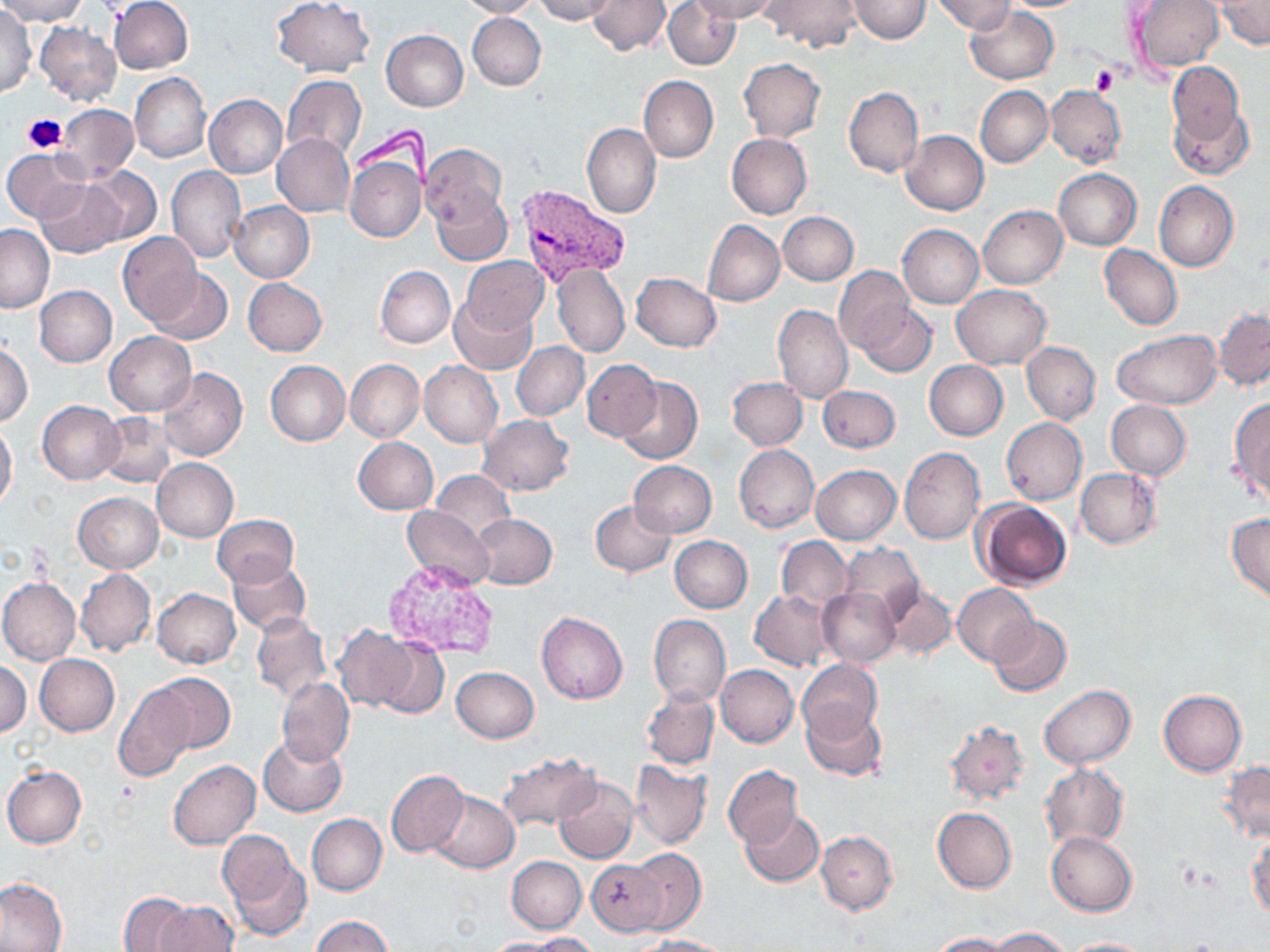

Summary:
  - Coordinate format: approximate bounding boxes as [x1, y1, x2, y2] in pixels
  - Platelet locations: [1090, 66, 1122, 94], [23, 113, 68, 153]
  - Uninfected red blood cell locations: [0, 0, 87, 24], [108, 0, 193, 74], [272, 0, 374, 76], [457, 0, 541, 18], [533, 0, 618, 23], [589, 0, 672, 55], [663, 0, 741, 70], [691, 0, 779, 22], [760, 0, 862, 53], [848, 0, 932, 42], [930, 0, 1014, 34], [1130, 1, 1222, 72], [1215, 1, 1269, 50], [967, 5, 1059, 83], [0, 8, 37, 98], [467, 13, 546, 90], [35, 21, 122, 105], [381, 30, 468, 112], [739, 58, 825, 141], [1168, 61, 1244, 145], [130, 72, 210, 162], [282, 75, 366, 160], [638, 76, 717, 162], [844, 85, 924, 178], [975, 85, 1053, 167], [1046, 85, 1126, 167], [204, 94, 288, 179], [58, 104, 137, 181], [1170, 104, 1254, 178], [583, 123, 661, 218], [900, 130, 989, 215], [272, 133, 355, 217], [726, 133, 811, 219], [420, 144, 507, 228], [3, 148, 90, 222], [345, 156, 426, 242], [86, 165, 162, 246], [167, 166, 246, 263], [1055, 169, 1142, 250], [36, 179, 127, 259], [1154, 180, 1238, 272], [431, 190, 513, 265], [230, 202, 314, 283], [977, 205, 1068, 289], [777, 211, 859, 285], [702, 220, 784, 306], [0, 224, 54, 312], [898, 224, 984, 308], [118, 232, 202, 326], [1100, 245, 1182, 330], [460, 257, 549, 334], [369, 264, 447, 428], [552, 264, 631, 358], [376, 266, 455, 347], [834, 266, 915, 355], [147, 268, 233, 346], [631, 273, 721, 351], [243, 277, 327, 356], [34, 285, 117, 367], [951, 285, 1052, 368], [449, 297, 539, 373], [856, 303, 937, 378], [773, 304, 853, 403], [1214, 308, 1270, 388], [1113, 330, 1222, 410], [104, 332, 196, 416], [511, 341, 589, 421], [1022, 342, 1100, 424], [0, 344, 32, 426], [265, 360, 350, 446], [346, 360, 424, 441], [582, 360, 661, 441], [420, 361, 503, 447], [924, 361, 1007, 440], [159, 367, 247, 461], [616, 375, 703, 465], [726, 376, 807, 450], [818, 385, 902, 453], [1229, 398, 1270, 500], [38, 400, 124, 485], [1106, 401, 1191, 479], [97, 413, 176, 487], [476, 414, 575, 496], [1002, 418, 1087, 505], [0, 422, 18, 508], [354, 436, 439, 514], [734, 444, 819, 533], [899, 447, 984, 545], [152, 457, 238, 542], [628, 460, 717, 537], [811, 465, 901, 544], [1076, 469, 1160, 548], [432, 471, 515, 544], [73, 493, 163, 573], [974, 499, 1073, 590], [591, 500, 676, 576], [404, 505, 494, 593], [1228, 513, 1270, 602], [471, 514, 557, 588], [213, 515, 297, 587], [775, 535, 852, 611], [669, 536, 752, 613], [837, 545, 925, 621], [229, 559, 310, 635], [75, 568, 156, 656], [0, 578, 80, 665], [883, 580, 956, 659], [954, 583, 1038, 666], [817, 587, 901, 667], [152, 588, 241, 668], [750, 591, 834, 671], [251, 612, 331, 702], [537, 612, 627, 704], [649, 615, 730, 707], [988, 617, 1071, 697], [331, 626, 418, 711], [372, 637, 448, 719], [35, 654, 119, 735], [798, 659, 881, 743], [0, 661, 30, 737], [716, 664, 799, 747], [451, 666, 539, 742], [151, 672, 234, 754], [276, 677, 354, 766], [115, 682, 194, 781], [1039, 685, 1136, 767], [642, 688, 719, 769], [1159, 690, 1247, 776], [801, 702, 885, 782], [943, 720, 1031, 806], [258, 735, 347, 817], [498, 752, 600, 830], [1221, 759, 1270, 843], [169, 761, 260, 849], [631, 761, 711, 849], [1039, 764, 1128, 850], [2, 765, 87, 849], [723, 765, 802, 848], [386, 770, 470, 858], [553, 777, 638, 864], [429, 790, 519, 873], [932, 807, 1017, 893], [741, 809, 824, 886], [307, 813, 386, 895], [1046, 831, 1137, 917], [817, 832, 896, 913], [1247, 833, 1269, 922], [220, 834, 310, 942], [628, 847, 706, 935], [507, 856, 586, 933], [585, 859, 668, 936], [0, 880, 70, 951], [120, 892, 196, 950], [150, 900, 238, 952], [311, 915, 393, 951], [990, 927, 1071, 951], [532, 932, 599, 951], [928, 933, 1013, 952], [642, 935, 732, 952], [1058, 937, 1154, 952], [482, 938, 569, 951]
  - Plasmodium vivax-infected red blood cell locations: [515, 183, 631, 289]
  - Slide-level diagnosis: Plasmodium vivax
  - Image size: 1270×952 pixels
  - Preparation: thin blood film
  - Modality: light microscopy
  - Stain: May-Grünwald-Giemsa
  - Magnification: 1000x
  - Field of view: single